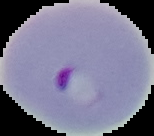

Summary:
  - Malaria status: parasitized
  - Image type: cell region segmented out of the field of view; surrounding area masked to black
  - Preparation: thin blood film
  - Image size: 154×136 pixels